Locate and identify every blood parasite.
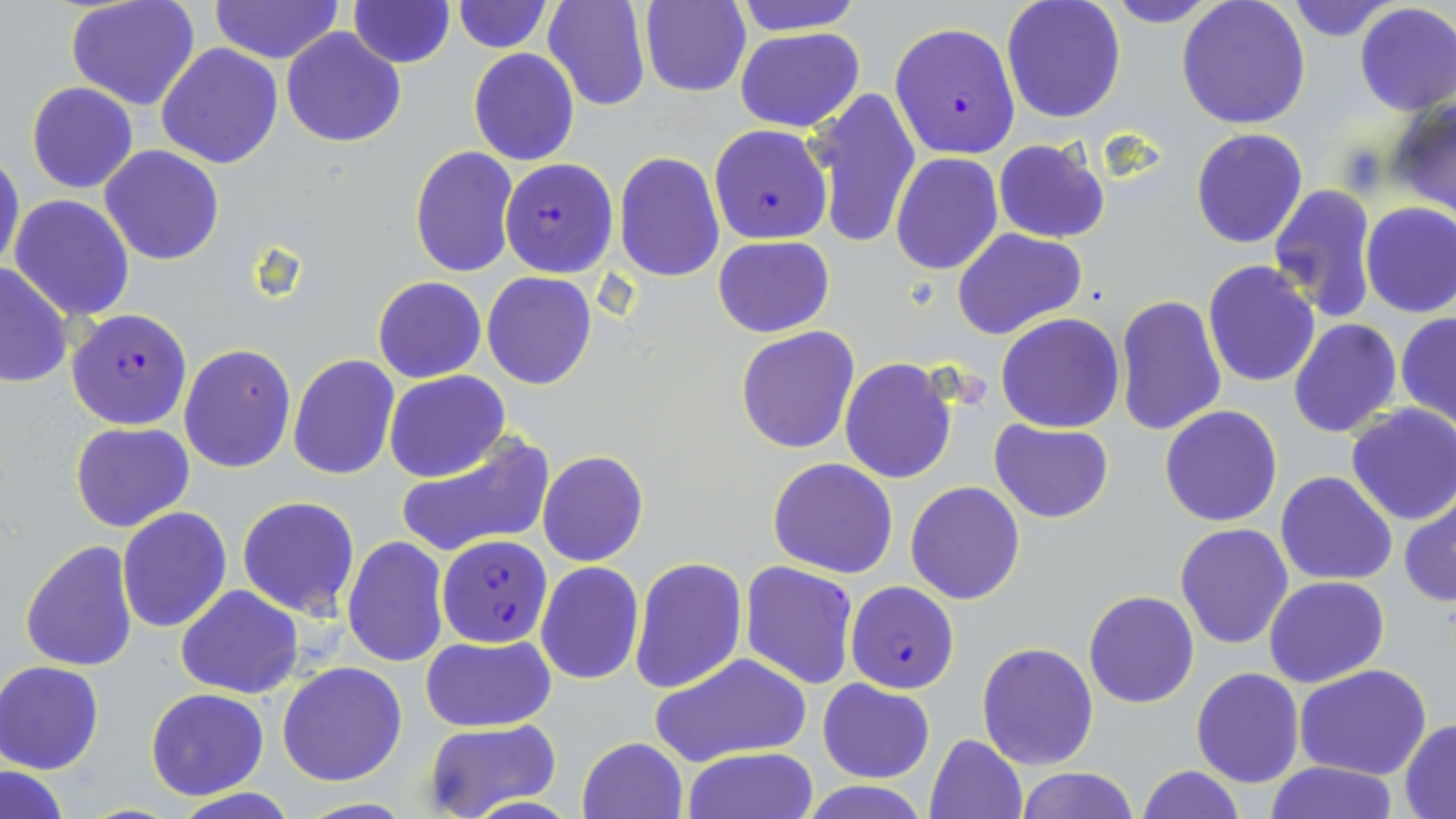

Approximate bounding boxes as (x1,y1)-(x2,y2) corner pairs in pixels.
Plasmodium falciparum-infected red blood cells: (890,21)-(1020,159), (708,124)-(832,245), (498,157)-(618,277), (66,307)-(193,430), (438,535)-(554,648), (739,559)-(859,689), (846,581)-(960,694).
No Plasmodium ovale, Plasmodium malariae, Plasmodium vivax, Babesia divergens, or Trypanosoma brucei observed.

Uninfected red blood cell locations: (65,0)-(202,111), (349,0)-(455,68), (542,0)-(652,113), (732,0)-(866,35), (1001,0)-(1127,122), (1103,0)-(1226,27), (1285,0)-(1398,41), (639,1)-(750,97), (1176,1)-(1312,134), (209,2)-(344,64), (453,2)-(552,53), (1354,3)-(1456,115), (732,26)-(867,132), (281,27)-(407,147), (156,43)-(284,169), (468,47)-(580,166), (25,82)-(139,195), (806,86)-(921,249), (1388,100)-(1456,219), (1190,127)-(1308,248), (992,138)-(1110,242), (99,145)-(225,265), (409,146)-(521,280), (0,151)-(25,277), (614,152)-(724,284), (891,153)-(1004,275), (1267,183)-(1379,324), (9,194)-(134,321), (1360,203)-(1456,319), (951,227)-(1088,341), (713,236)-(834,337), (1203,259)-(1320,388), (0,260)-(75,389), (482,271)-(597,390), (372,277)-(486,384), (1115,294)-(1227,436), (995,311)-(1126,433), (1396,313)-(1456,429), (1287,318)-(1402,439), (735,326)-(860,453), (178,343)-(297,473), (287,355)-(400,480), (838,359)-(958,485), (384,371)-(509,482), (1345,403)-(1456,525), (1158,404)-(1283,528), (988,419)-(1112,523), (71,421)-(194,532), (395,435)-(554,558), (538,450)-(648,567), (768,458)-(898,577), (1275,470)-(1397,586), (906,481)-(1027,604), (1399,494)-(1456,607), (237,495)-(361,620), (117,507)-(232,631), (1173,522)-(1294,650), (342,537)-(449,667), (19,539)-(140,672), (629,555)-(746,695), (535,562)-(645,683), (1264,575)-(1390,688), (175,584)-(303,698), (1083,590)-(1200,708), (422,634)-(556,733), (976,641)-(1101,771), (653,651)-(812,766), (0,660)-(105,774), (277,662)-(406,787), (1295,665)-(1432,781), (1191,667)-(1304,788), (819,680)-(934,783), (145,688)-(269,800), (1401,719)-(1456,815), (421,720)-(563,818), (924,733)-(1028,819), (577,736)-(688,819), (680,747)-(820,819), (1262,760)-(1400,819), (1,765)-(72,819), (1135,765)-(1245,819), (1014,766)-(1137,819), (800,779)-(927,817). Slide-level diagnosis: Plasmodium falciparum. Image is 1456×819 pixels. Light microscopy. 1000x magnification. May-Grünwald-Giemsa-stained preparation. One field of a larger specimen. Thin blood smear.